Classify this cell by malaria status.
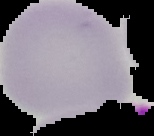
Uninfected.

Cell region segmented out of the field of view; the surrounding area is masked to black. Image is 154×136 pixels. From a thin blood smear.